Report the malaria status of this cell.
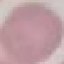

It is uninfected.

Thin blood smear. Photographed with a smartphone camera at the microscope eyepiece. Giemsa stain. Automatically extracted cell patch, resized to 64 × 64 pixels.